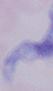 Photomicrograph. A trypanosome is seen. 1000x magnification.